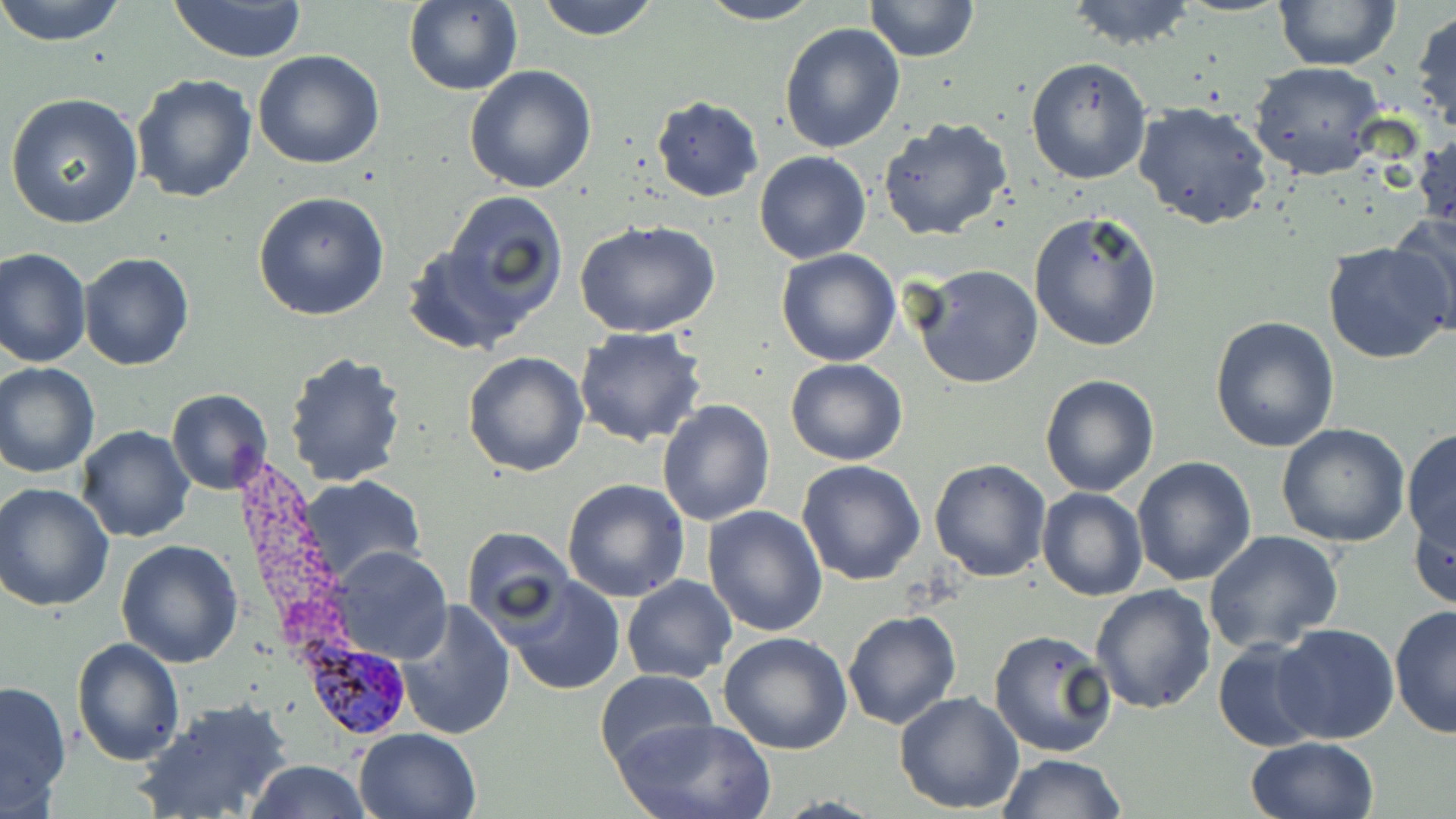 Approximate bounding boxes as named x1/y1/x2/y2 corners in pixels. Uninfected red blood cell locations: (x1=0, y1=0, x2=128, y2=47), (x1=165, y1=0, x2=310, y2=64), (x1=534, y1=0, x2=661, y2=41), (x1=695, y1=0, x2=825, y2=25), (x1=864, y1=0, x2=980, y2=62), (x1=1062, y1=0, x2=1200, y2=50), (x1=404, y1=1, x2=524, y2=97), (x1=1275, y1=1, x2=1400, y2=71), (x1=1410, y1=7, x2=1456, y2=138), (x1=779, y1=21, x2=906, y2=154), (x1=252, y1=49, x2=386, y2=169), (x1=1025, y1=57, x2=1152, y2=186), (x1=1248, y1=61, x2=1385, y2=179), (x1=465, y1=64, x2=598, y2=193), (x1=131, y1=74, x2=258, y2=206), (x1=5, y1=93, x2=144, y2=230), (x1=650, y1=97, x2=764, y2=201), (x1=1133, y1=101, x2=1276, y2=232), (x1=877, y1=119, x2=1014, y2=242), (x1=1413, y1=127, x2=1455, y2=243), (x1=754, y1=151, x2=870, y2=263), (x1=444, y1=190, x2=569, y2=311), (x1=252, y1=191, x2=390, y2=322), (x1=1028, y1=210, x2=1165, y2=352), (x1=1389, y1=210, x2=1456, y2=334), (x1=575, y1=219, x2=721, y2=338), (x1=401, y1=238, x2=543, y2=354), (x1=1322, y1=241, x2=1455, y2=364), (x1=1, y1=247, x2=91, y2=367), (x1=775, y1=248, x2=902, y2=367), (x1=78, y1=251, x2=194, y2=371), (x1=910, y1=263, x2=1043, y2=390), (x1=1209, y1=314, x2=1340, y2=452), (x1=574, y1=326, x2=709, y2=448), (x1=282, y1=350, x2=410, y2=488), (x1=463, y1=350, x2=590, y2=477), (x1=787, y1=358, x2=908, y2=467), (x1=0, y1=362, x2=100, y2=476), (x1=1040, y1=375, x2=1158, y2=496), (x1=167, y1=388, x2=274, y2=494), (x1=657, y1=399, x2=776, y2=525), (x1=1276, y1=423, x2=1410, y2=548), (x1=76, y1=425, x2=196, y2=544), (x1=1403, y1=429, x2=1456, y2=556), (x1=1132, y1=456, x2=1257, y2=588), (x1=929, y1=458, x2=1053, y2=582), (x1=795, y1=460, x2=925, y2=586), (x1=296, y1=475, x2=426, y2=588), (x1=562, y1=479, x2=691, y2=603), (x1=2, y1=483, x2=116, y2=613), (x1=1037, y1=487, x2=1147, y2=601), (x1=1410, y1=501, x2=1456, y2=612), (x1=703, y1=505, x2=828, y2=637), (x1=462, y1=527, x2=575, y2=631), (x1=1202, y1=530, x2=1344, y2=654), (x1=114, y1=539, x2=244, y2=667), (x1=329, y1=548, x2=451, y2=664), (x1=622, y1=575, x2=737, y2=684), (x1=503, y1=576, x2=627, y2=696), (x1=1090, y1=586, x2=1217, y2=716), (x1=396, y1=600, x2=517, y2=740), (x1=1390, y1=602, x2=1456, y2=741), (x1=843, y1=611, x2=962, y2=730), (x1=1272, y1=624, x2=1400, y2=745), (x1=987, y1=628, x2=1119, y2=760), (x1=720, y1=630, x2=853, y2=754), (x1=1213, y1=636, x2=1326, y2=753), (x1=71, y1=637, x2=185, y2=766), (x1=595, y1=670, x2=718, y2=774), (x1=0, y1=680, x2=72, y2=812), (x1=895, y1=691, x2=1024, y2=813), (x1=135, y1=698, x2=294, y2=819), (x1=614, y1=717, x2=776, y2=818), (x1=353, y1=727, x2=481, y2=818), (x1=1245, y1=736, x2=1380, y2=819), (x1=998, y1=752, x2=1129, y2=818), (x1=247, y1=759, x2=370, y2=818). Plasmodium ovale-infected red blood cell locations: (x1=300, y1=638, x2=412, y2=742). Slide-level diagnosis: Plasmodium ovale. Image is 1456×819 pixels. One field of a larger specimen. Thin blood film. May-Grünwald-Giemsa stain. Optical microscopy. Captured at 1000x magnification.